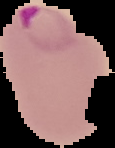
image type = segmented cell region on a black background
malaria status = parasitized
image size = 115×148 pixels
preparation = thin blood film